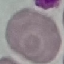
Summary:
  - Malaria status: uninfected
  - Capture: smartphone through the microscope eyepiece
  - Image type: cell patch, automatically extracted from a larger field of view and resized to 64 × 64 pixels
  - Preparation: thin blood film
  - Stain: Giemsa